Identify the parasite.
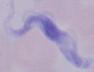

A trypanosome.

magnification = 1000x
modality = micrograph